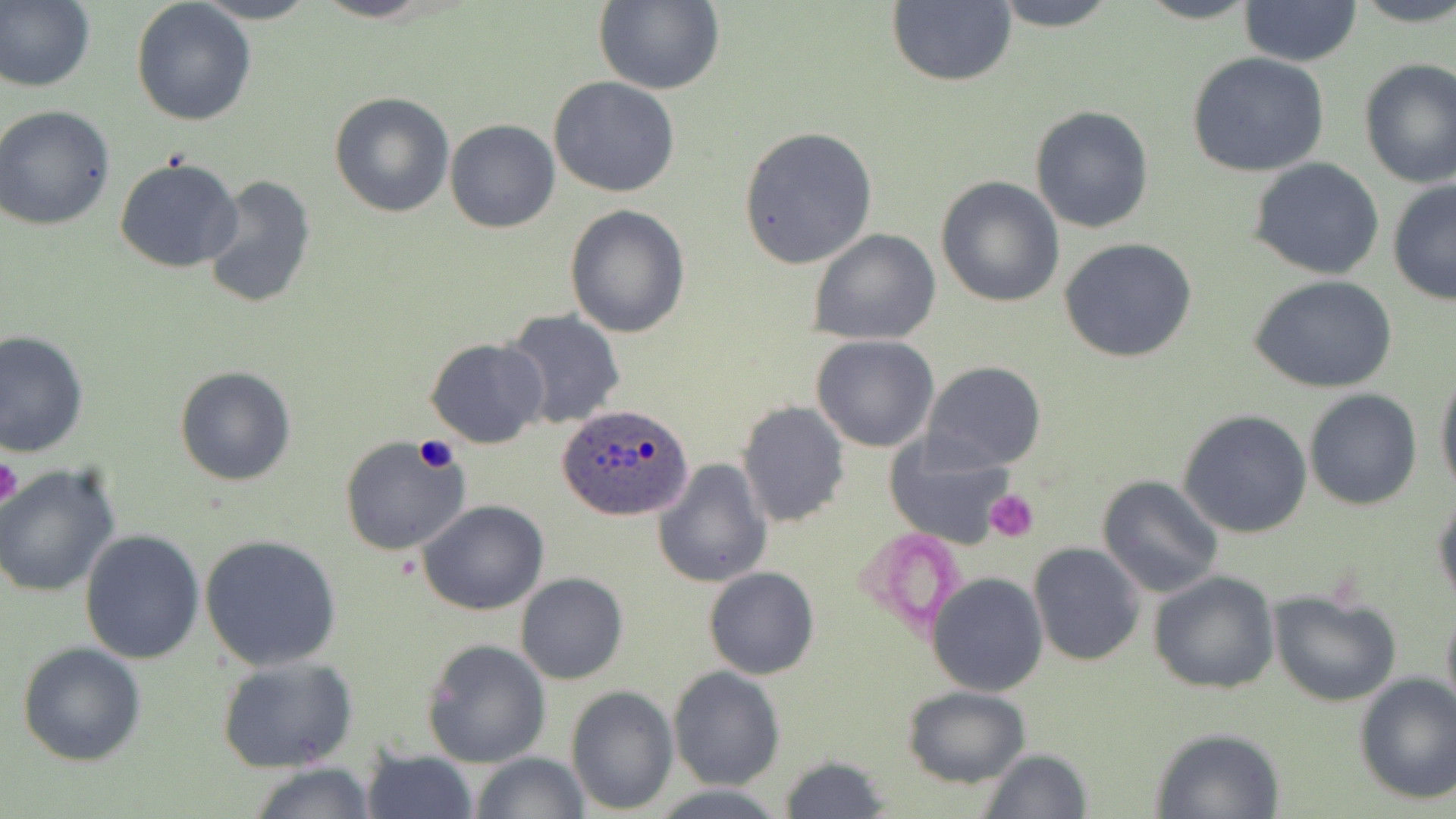
slide-level diagnosis = Plasmodium ovale
stain = May-Grünwald-Giemsa
field of view = single
preparation = thin blood smear
magnification = 1000x
image size = 1456×819 pixels
Plasmodium ovale-infected red blood cell locations = approximate bounding boxes as [x1, y1, x2, y2] in pixels: [557, 403, 695, 521]
uninfected red blood cell locations = approximate bounding boxes as [x1, y1, x2, y2] in pixels: [0, 0, 95, 93], [192, 0, 319, 24], [312, 0, 439, 23], [988, 0, 1123, 31], [1128, 0, 1265, 25], [1348, 0, 1456, 28], [593, 1, 724, 94], [885, 1, 1016, 87], [1238, 1, 1361, 67], [131, 2, 257, 128], [1185, 52, 1331, 177], [1358, 59, 1455, 190], [548, 76, 680, 198], [329, 91, 455, 218], [0, 104, 115, 231], [1029, 105, 1154, 234], [445, 120, 560, 233], [738, 126, 878, 269], [114, 156, 243, 273], [1248, 157, 1384, 279], [201, 174, 317, 311], [935, 174, 1065, 307], [1387, 178, 1456, 306], [564, 205, 690, 339], [808, 229, 942, 346], [1058, 237, 1199, 364], [1247, 274, 1398, 394], [502, 309, 626, 430], [0, 330, 89, 461], [810, 334, 939, 452], [426, 337, 549, 449], [922, 361, 1046, 472], [1435, 364, 1456, 501], [175, 365, 296, 486], [1303, 389, 1424, 510], [736, 399, 850, 527], [1177, 408, 1313, 538], [882, 433, 1016, 552], [339, 436, 469, 556], [653, 457, 773, 589], [0, 462, 123, 599], [1097, 474, 1223, 597], [1432, 490, 1456, 611], [418, 500, 549, 617], [78, 529, 205, 665], [198, 533, 343, 672], [1027, 543, 1145, 666], [703, 567, 819, 680], [1148, 570, 1281, 695], [516, 572, 629, 685], [926, 572, 1049, 697], [1267, 589, 1402, 708], [1440, 599, 1456, 728], [422, 638, 550, 767], [17, 641, 148, 767], [216, 655, 359, 772], [668, 666, 784, 790], [1353, 673, 1456, 806], [567, 684, 678, 814], [901, 686, 1031, 787], [1151, 727, 1284, 817], [360, 745, 479, 819], [979, 748, 1091, 819], [471, 751, 588, 819], [780, 754, 891, 817], [247, 762, 379, 819]
platelet locations = approximate bounding boxes as [x1, y1, x2, y2] in pixels: [412, 437, 459, 472], [0, 454, 23, 512], [985, 490, 1037, 540]
modality = optical microscopy